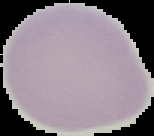

Summary:
  - Preparation: thin blood film
  - Image type: cell region segmented out of the field of view; surrounding area masked to black
  - Malaria status: uninfected
  - Image size: 154×136 pixels